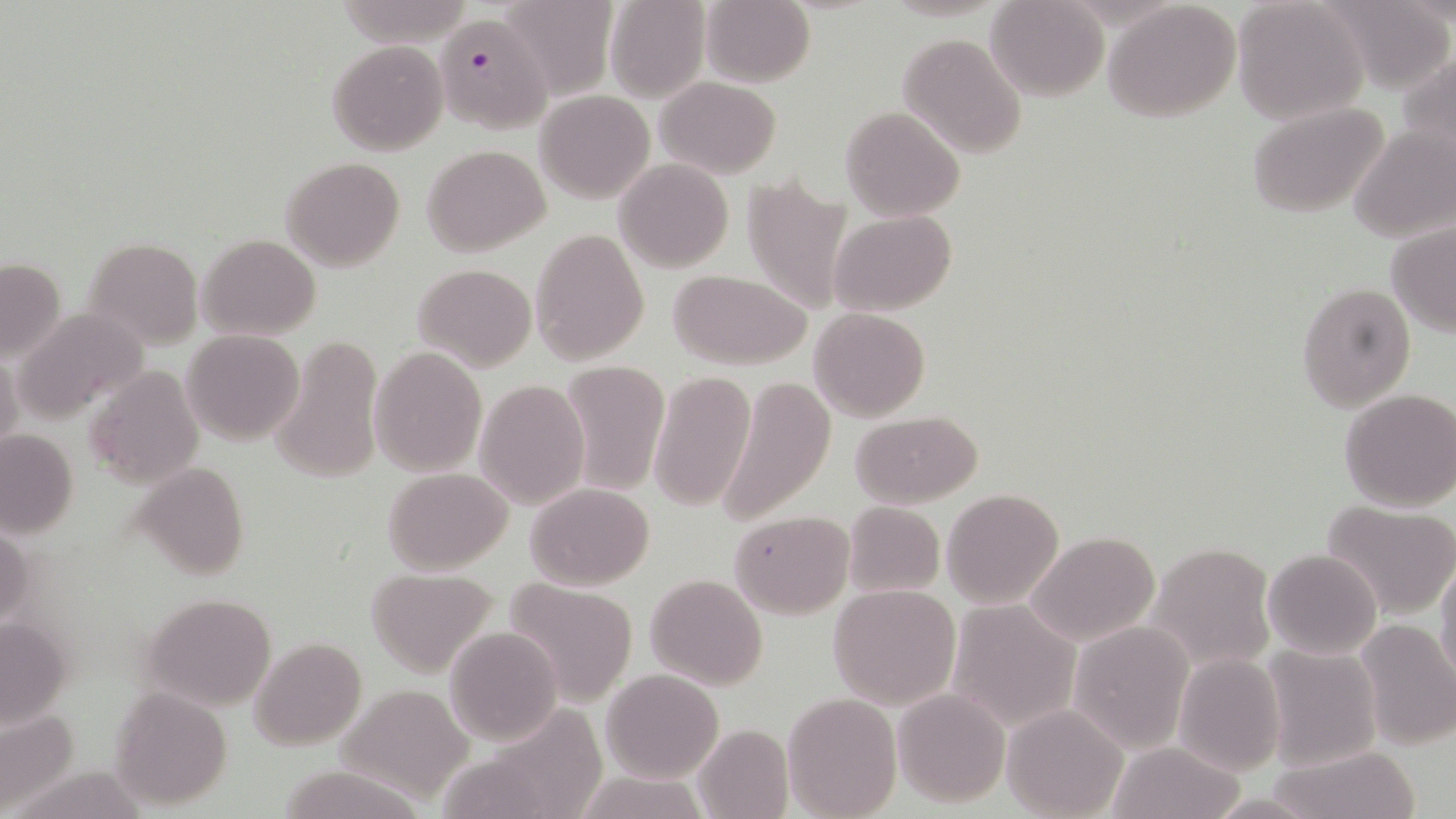

slide-level diagnosis = Plasmodium falciparum
image size = 1456×819 pixels
uninfected red blood cell locations = approximate bounding boxes as (x1,y1)-(x2,y2) corner pairs in pixels: (337,0)-(477,49), (497,0)-(619,96), (604,0)-(710,103), (700,0)-(815,87), (984,1)-(1108,102), (1103,1)-(1243,121), (1231,1)-(1367,124), (897,33)-(1028,157), (328,39)-(448,155), (1399,48)-(1456,169), (654,77)-(782,178), (536,90)-(654,202), (1248,100)-(1393,220), (840,106)-(965,220), (1349,126)-(1455,243), (423,145)-(549,258), (282,157)-(404,272), (614,159)-(735,273), (740,173)-(854,314), (829,210)-(957,317), (1386,218)-(1456,337), (530,226)-(650,366), (198,234)-(321,340), (81,237)-(202,351), (0,257)-(65,362), (413,262)-(537,370), (667,270)-(814,370), (1296,282)-(1415,410), (12,308)-(151,423), (809,308)-(929,422), (181,330)-(304,445), (270,336)-(382,483), (370,347)-(488,477), (0,348)-(23,456), (557,360)-(670,496), (84,366)-(205,490), (647,369)-(754,513), (716,377)-(836,526), (474,379)-(590,509), (1339,388)-(1456,512), (850,409)-(983,508), (0,428)-(79,539), (133,463)-(250,581), (383,467)-(514,574), (524,482)-(655,589), (942,489)-(1066,610), (1321,501)-(1456,620), (841,502)-(945,598), (728,509)-(854,618), (0,522)-(31,632), (1025,531)-(1160,646), (1148,541)-(1275,670), (1262,549)-(1381,660), (1436,555)-(1456,690), (365,568)-(499,677), (645,573)-(769,689), (502,577)-(639,704), (827,584)-(961,709), (138,593)-(276,710), (945,599)-(1080,733), (0,614)-(76,731), (1353,619)-(1456,750), (1068,620)-(1196,755), (445,626)-(564,746), (249,637)-(365,751), (1260,645)-(1382,770), (1173,653)-(1285,776), (601,668)-(724,782), (336,682)-(477,802), (892,687)-(1010,808), (108,688)-(232,808), (783,691)-(900,818), (0,704)-(83,812), (1001,704)-(1127,818), (693,722)-(793,819), (1105,741)-(1246,819), (1269,744)-(1422,819), (271,763)-(431,819), (574,772)-(710,817)
Plasmodium falciparum-infected red blood cell locations = approximate bounding boxes as (x1,y1)-(x2,y2) corner pairs in pixels: (434,13)-(551,132)
field of view = one of a larger specimen
stain = May-Grünwald-Giemsa
magnification = 1000x
preparation = thin blood smear
modality = optical microscopy